Report the malaria status of this cell.
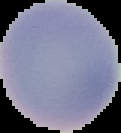

It is uninfected.

Summary:
  - Image size: 121×133 pixels
  - Image type: cell region segmented out of the field of view; surrounding area masked to black
  - Preparation: thin blood film